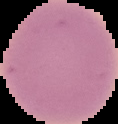
Result: negative for malaria parasites. Cell region segmented out of the field of view; the surrounding area is masked to black. Image is 118×124 pixels. From a thin blood smear.